Assess this cell for malaria.
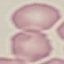
It is uninfected.

Giemsa stain. Cell patch, automatically extracted from a larger field of view and resized to 64 × 64 pixels. Thin blood smear. Photographed with a smartphone camera at the microscope eyepiece.